Report the malaria status of this cell.
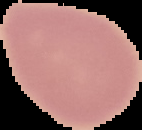
It is uninfected.

From a thin blood smear. The area outside the segmented cell region is set to black. Image is 142×130 pixels.